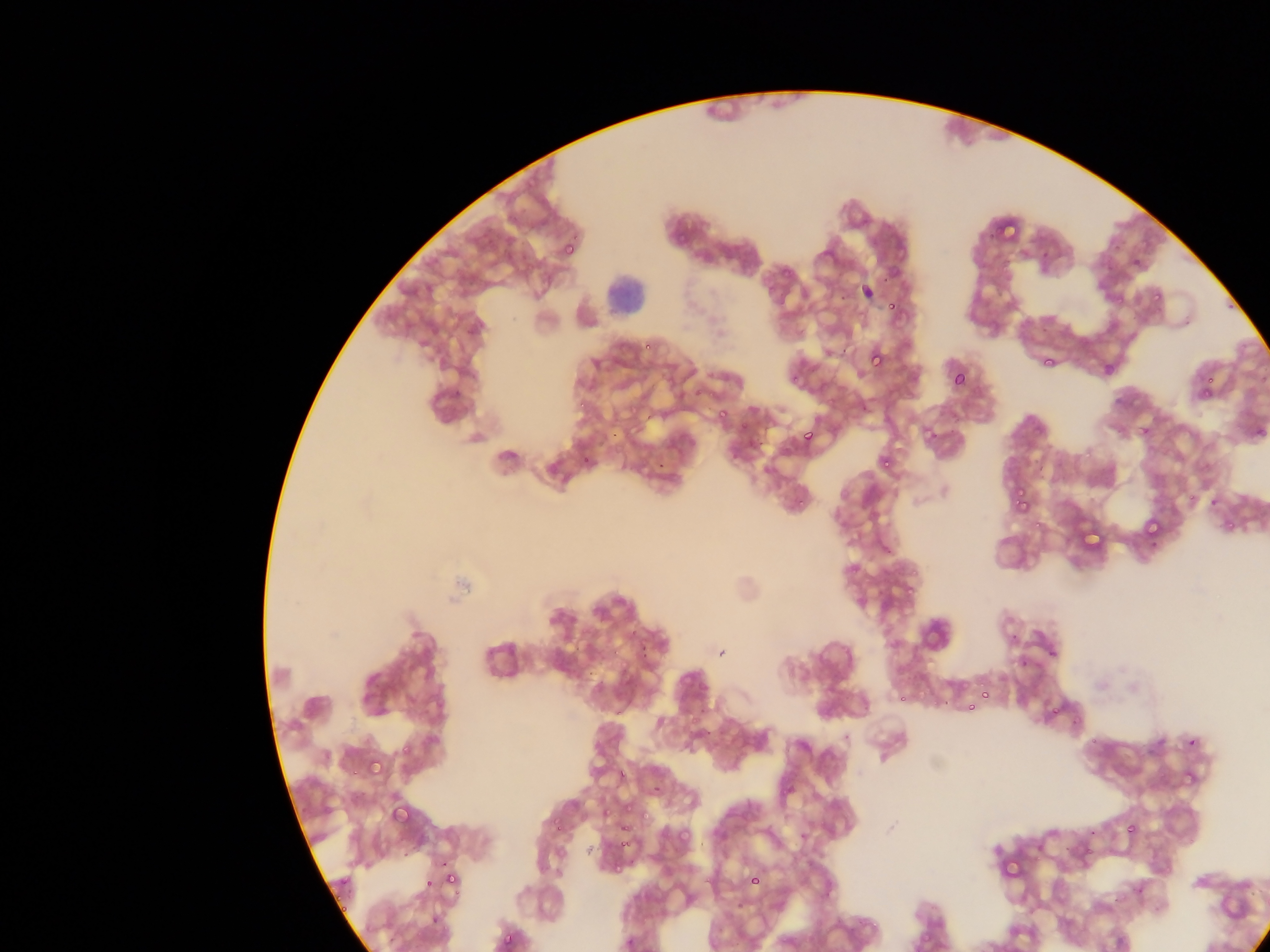

Approximate bounding boxes as [left, top, right, bottom] in pixels.
Summary:
  - Malaria parasite locations: [673, 230, 686, 243], [675, 234, 689, 246], [564, 235, 582, 254], [562, 241, 577, 258], [881, 275, 890, 284], [1151, 290, 1164, 303], [1114, 293, 1126, 305], [887, 301, 898, 312], [644, 341, 654, 350], [869, 350, 885, 368], [1042, 354, 1058, 369], [952, 371, 966, 387], [791, 373, 802, 383], [1206, 374, 1216, 389], [1200, 385, 1213, 399], [577, 400, 586, 410], [718, 408, 728, 419], [738, 420, 747, 430], [1139, 424, 1152, 437], [1254, 427, 1267, 439], [804, 431, 815, 442], [581, 452, 591, 467], [880, 455, 898, 470], [656, 460, 665, 468], [1014, 487, 1025, 498], [1185, 493, 1195, 501], [1207, 497, 1222, 505], [1016, 499, 1030, 512], [1143, 518, 1161, 537], [1224, 520, 1235, 531], [903, 582, 917, 598], [638, 644, 649, 661], [1047, 647, 1059, 658], [613, 648, 620, 661], [1019, 659, 1029, 668], [982, 691, 990, 699], [896, 694, 905, 703], [968, 702, 977, 712], [1050, 705, 1062, 717], [695, 706, 708, 717], [706, 731, 715, 735], [1091, 738, 1100, 747], [1188, 738, 1197, 747], [401, 742, 414, 756], [366, 757, 384, 776], [350, 767, 358, 780], [617, 768, 628, 779], [626, 801, 634, 815], [393, 804, 411, 821], [602, 808, 611, 818], [641, 810, 651, 821], [553, 821, 564, 833], [619, 823, 629, 832], [1126, 823, 1137, 834], [676, 828, 691, 844], [620, 839, 628, 848], [1084, 849, 1092, 859], [402, 853, 408, 862], [437, 860, 449, 868], [336, 870, 347, 882], [443, 871, 456, 885], [747, 874, 761, 887], [425, 880, 433, 889], [339, 903, 348, 913], [431, 908, 445, 925], [499, 930, 517, 948] | approximate [x, y] pixel centers of objects too small to bound: [658, 787]
  - Leukocyte locations: [602, 271, 644, 311]
  - Field of view: single
  - Image size: 1270×952 pixels
  - Preparation: thin blood smear
  - Country: Ghana
  - Capture: mobile-phone photograph through a microscope